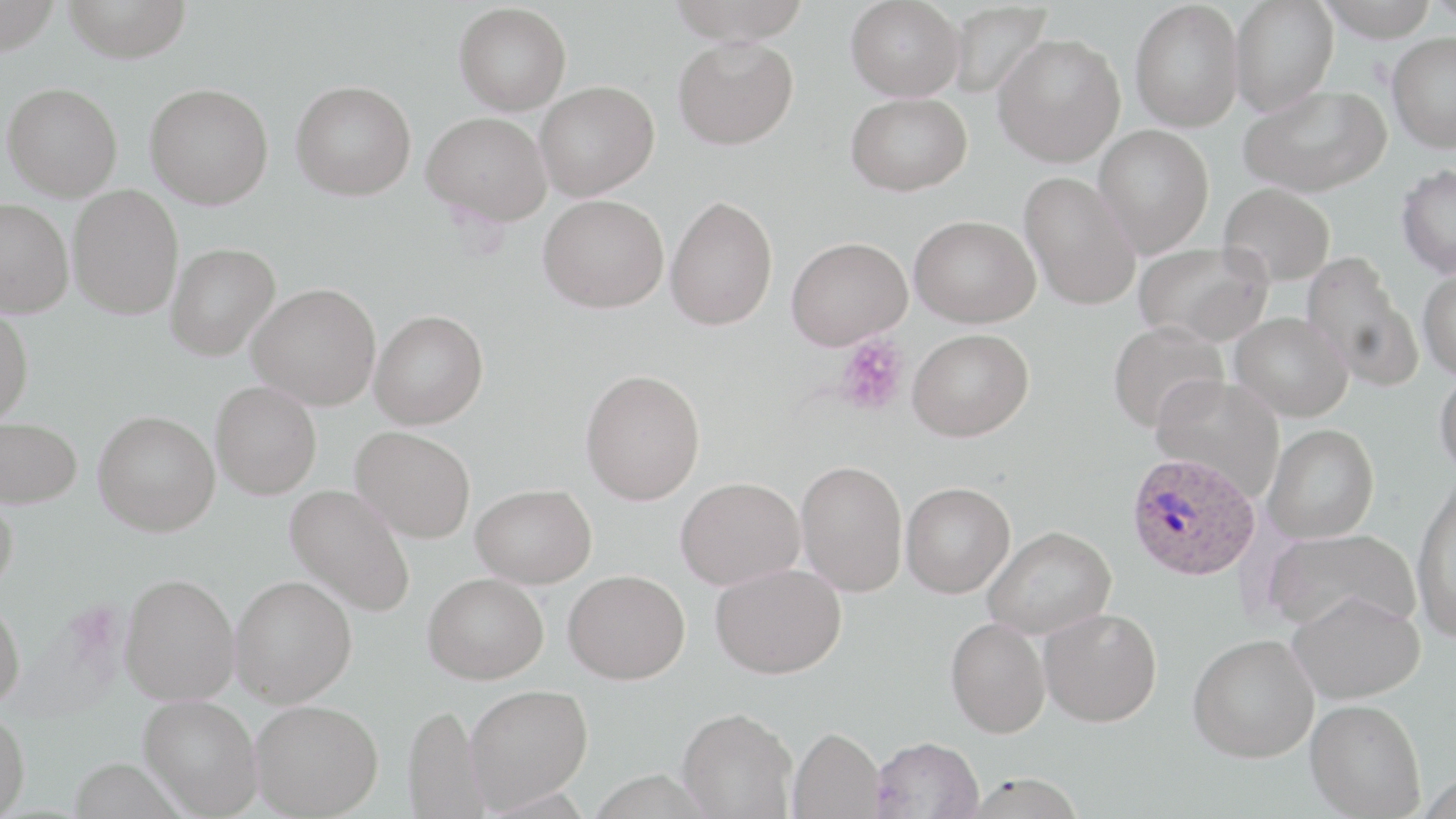

Summary:
  - Coordinate format: approximate bounding boxes as [x1, y1, x2, y2] in pixels
  - Uninfected red blood cell locations: [0, 0, 62, 55], [62, 0, 192, 62], [664, 0, 814, 44], [845, 0, 966, 101], [1229, 0, 1339, 117], [1318, 0, 1439, 41], [1130, 1, 1244, 133], [1419, 1, 1456, 23], [454, 2, 572, 115], [945, 3, 1052, 101], [1387, 32, 1456, 153], [992, 33, 1126, 167], [673, 36, 799, 150], [291, 79, 417, 201], [535, 80, 659, 200], [2, 82, 123, 201], [145, 82, 274, 209], [1238, 84, 1391, 197], [846, 92, 972, 196], [422, 111, 551, 225], [1093, 125, 1214, 258], [1396, 164, 1456, 279], [1019, 171, 1141, 311], [1218, 182, 1336, 286], [67, 184, 184, 320], [538, 194, 669, 312], [665, 195, 778, 331], [0, 198, 74, 318], [910, 214, 1039, 327], [787, 236, 912, 350], [1133, 241, 1274, 346], [165, 243, 280, 361], [1301, 251, 1421, 390], [1417, 267, 1456, 380], [247, 282, 381, 410], [0, 304, 34, 426], [370, 309, 489, 429], [1230, 312, 1353, 421], [1108, 321, 1229, 431], [907, 328, 1033, 441], [1434, 366, 1456, 478], [580, 369, 705, 505], [1150, 374, 1285, 498], [211, 381, 322, 499], [93, 410, 220, 536], [0, 416, 83, 509], [1263, 424, 1379, 543], [351, 426, 476, 543], [796, 459, 908, 596], [676, 476, 805, 589], [1412, 480, 1456, 641], [901, 482, 1015, 598], [471, 483, 597, 588], [285, 484, 416, 616], [0, 489, 18, 597], [983, 525, 1116, 639], [1263, 528, 1420, 635], [711, 564, 846, 679], [563, 569, 690, 684], [119, 572, 239, 705], [423, 572, 548, 683], [230, 575, 357, 707], [1288, 589, 1425, 703], [0, 595, 25, 711], [1038, 607, 1162, 727], [945, 616, 1050, 737], [1188, 634, 1319, 763], [464, 684, 593, 810], [139, 694, 263, 817], [1305, 698, 1426, 818], [250, 699, 383, 818], [403, 701, 492, 819], [677, 707, 797, 818], [0, 708, 30, 819], [789, 726, 885, 818], [872, 736, 984, 819], [963, 772, 1088, 818]
  - Plasmodium ovale-infected red blood cell locations: [1127, 452, 1260, 580]
  - Platelet locations: [835, 336, 908, 416]
  - Slide-level diagnosis: Plasmodium ovale
  - Preparation: thin blood smear
  - Field of view: one of a larger specimen
  - Modality: light microscopy
  - Image size: 1456×819 pixels
  - Magnification: 1000x
  - Stain: May-Grünwald-Giemsa